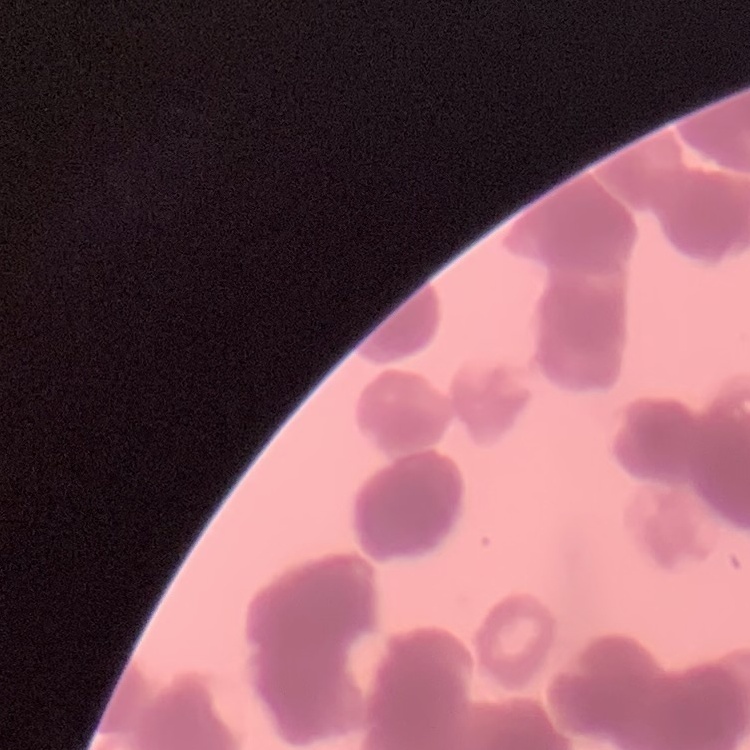
erythrocyte_morphology: rouleaux formation
preparation: thin peripheral smear
image_type: square crop of a larger photomicrograph
stain: Field's or Giemsa